Classify this cell by malaria status.
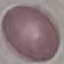
Uninfected.

preparation = thin blood film
stain = Giemsa
image type = cell patch, automatically extracted from a larger field of view and resized to 64 × 64 pixels
capture = smartphone through the microscope eyepiece